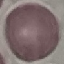

malaria status = uninfected
preparation = thin blood smear
image type = cell patch, automatically extracted from a larger field of view and resized to 64 × 64 pixels
stain = Giemsa
capture = smartphone through the microscope eyepiece